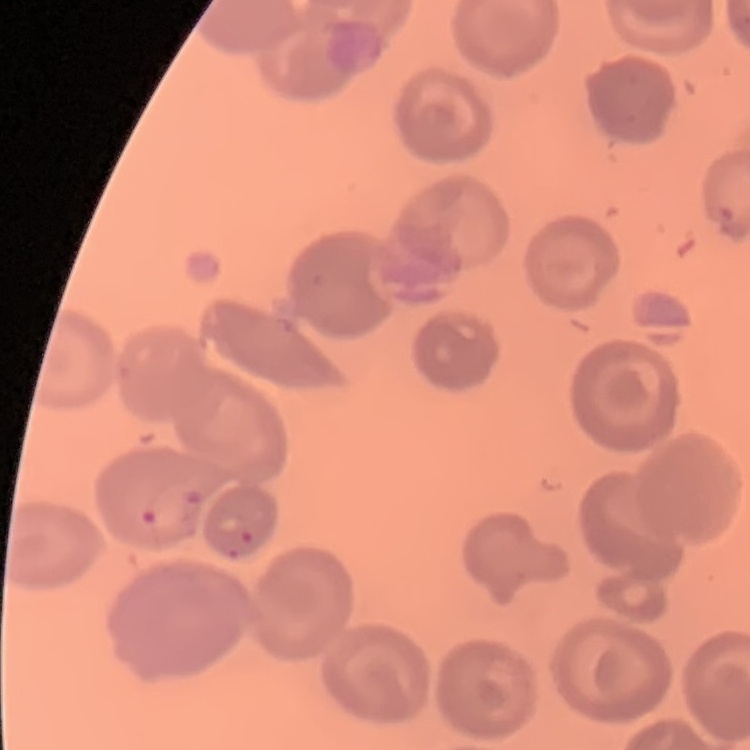

red blood cell morphology = no rouleaux formation
stain = Field's or Giemsa
preparation = thin blood film
image type = one tile cut from a larger photomicrograph